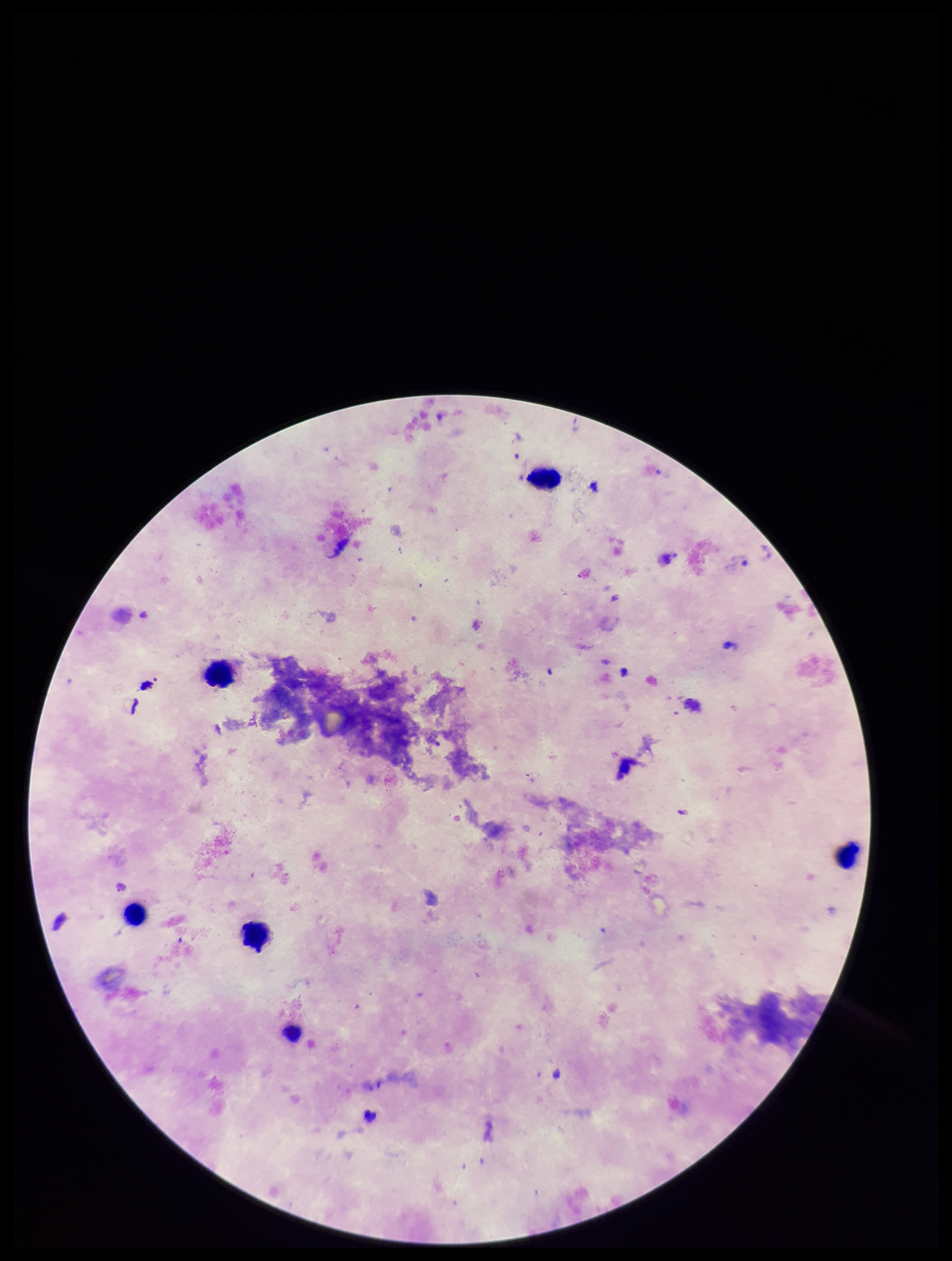 Giemsa stain. Leukocyte count: 5. Smartphone photograph taken through the eyepiece of a microscope. Preparation: thick smear. Plasmodium parasites: none identified. Image is 952×1261 pixels. Single field of view. Parasite count: 0. Patient malaria status: negative.